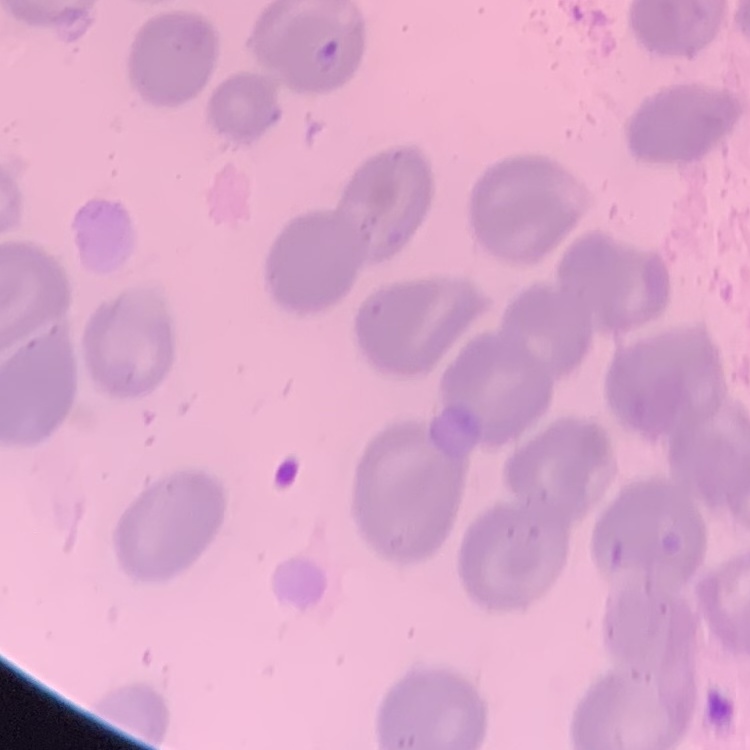
The erythrocytes show no rouleaux formation. Square crop of a larger photomicrograph. Thin peripheral smear. Stained with either Field's or Giemsa.